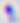
Summary:
  - Modality: micrograph
  - Magnification: 400x
  - Identification: Toxoplasma gondii